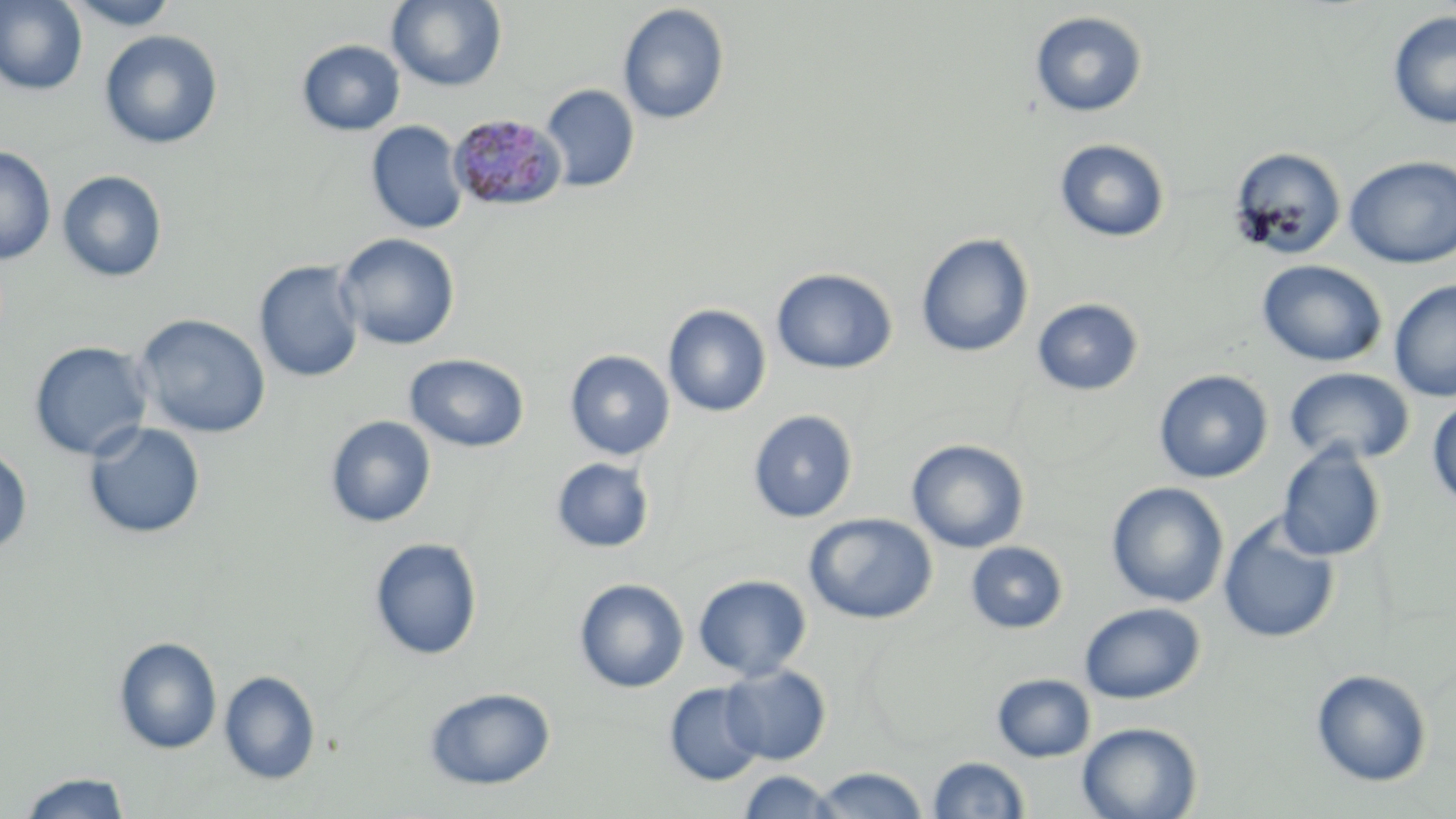
Summary:
  - Coordinate format: approximate bounding boxes as named x1/y1/x2/y2 corners in pixels
  - Plasmodium malariae-infected red blood cell locations: (x1=448, y1=112, x2=566, y2=212)
  - Uninfected red blood cell locations: (x1=64, y1=0, x2=181, y2=30), (x1=386, y1=0, x2=508, y2=91), (x1=0, y1=1, x2=88, y2=96), (x1=617, y1=4, x2=730, y2=125), (x1=1388, y1=10, x2=1456, y2=129), (x1=1029, y1=11, x2=1148, y2=117), (x1=99, y1=29, x2=223, y2=150), (x1=296, y1=39, x2=406, y2=136), (x1=541, y1=84, x2=640, y2=192), (x1=366, y1=121, x2=468, y2=234), (x1=1054, y1=138, x2=1171, y2=243), (x1=0, y1=146, x2=56, y2=265), (x1=1229, y1=147, x2=1348, y2=260), (x1=1344, y1=156, x2=1456, y2=267), (x1=57, y1=170, x2=168, y2=282), (x1=335, y1=233, x2=460, y2=351), (x1=915, y1=233, x2=1034, y2=358), (x1=1257, y1=259, x2=1388, y2=367), (x1=253, y1=260, x2=365, y2=383), (x1=771, y1=268, x2=898, y2=375), (x1=1389, y1=279, x2=1456, y2=402), (x1=1031, y1=297, x2=1144, y2=396), (x1=663, y1=304, x2=771, y2=417), (x1=133, y1=313, x2=271, y2=439), (x1=28, y1=340, x2=153, y2=461), (x1=564, y1=350, x2=675, y2=461), (x1=404, y1=353, x2=529, y2=453), (x1=1284, y1=367, x2=1415, y2=466), (x1=1153, y1=369, x2=1274, y2=483), (x1=1427, y1=397, x2=1456, y2=510), (x1=748, y1=409, x2=859, y2=523), (x1=324, y1=415, x2=436, y2=528), (x1=83, y1=420, x2=206, y2=540), (x1=906, y1=439, x2=1030, y2=554), (x1=1276, y1=443, x2=1388, y2=562), (x1=0, y1=444, x2=33, y2=556), (x1=550, y1=457, x2=655, y2=553), (x1=1106, y1=481, x2=1230, y2=608), (x1=804, y1=512, x2=938, y2=625), (x1=1217, y1=514, x2=1341, y2=644), (x1=369, y1=536, x2=483, y2=660), (x1=965, y1=542, x2=1069, y2=634), (x1=693, y1=574, x2=812, y2=681), (x1=573, y1=577, x2=689, y2=693), (x1=1079, y1=602, x2=1206, y2=704), (x1=113, y1=637, x2=222, y2=755), (x1=721, y1=664, x2=832, y2=765), (x1=1310, y1=668, x2=1433, y2=787), (x1=219, y1=669, x2=321, y2=785), (x1=991, y1=673, x2=1096, y2=762), (x1=664, y1=681, x2=767, y2=787), (x1=424, y1=686, x2=556, y2=790), (x1=1077, y1=721, x2=1202, y2=819), (x1=927, y1=756, x2=1031, y2=817), (x1=811, y1=766, x2=929, y2=818), (x1=737, y1=769, x2=838, y2=818), (x1=17, y1=771, x2=131, y2=818)
  - Slide-level diagnosis: Plasmodium malariae
  - Preparation: thin blood film
  - Field of view: one of a larger specimen
  - Modality: light microscopy
  - Stain: May-Grünwald-Giemsa
  - Magnification: 1000x
  - Image size: 1456×819 pixels